Classify this cell by malaria status.
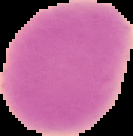
Uninfected.

image type = segmented cell region with the area outside set to black
image size = 133×136 pixels
preparation = thin blood film